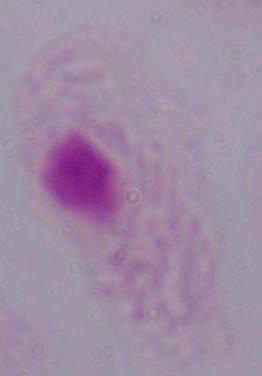 Micrograph. A trichomonad is shown. Captured at 1000x magnification.